Assess this cell for malaria.
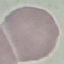

It is uninfected.

Summary:
  - Image type: automatically extracted cell patch, resized to 64 × 64 pixels
  - Capture: smartphone camera at the microscope eyepiece
  - Preparation: thin blood smear
  - Stain: Giemsa